Assess this cell for malaria.
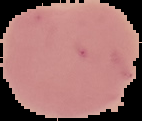

It is uninfected.

Image is 142×121 pixels. Cell region segmented out of the field of view; the surrounding area is masked to black. From a thin blood film.